Report the malaria status of this cell.
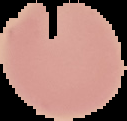
Uninfected.

Summary:
  - Image type: segmented cell region with the area outside set to black
  - Image size: 127×121 pixels
  - Preparation: thin blood smear